Report the malaria status of this cell.
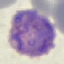

Parasitized.

Cell patch, automatically extracted from a larger field of view and resized to 64 × 64 pixels. Thin blood smear. Giemsa-stained preparation. Acquired by smartphone through the microscope eyepiece.